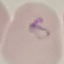
Summary:
  - Result: malaria parasites detected
  - Preparation: thin smear
  - Image type: automatically extracted cell patch, resized to 64 × 64 pixels
  - Stain: Giemsa
  - Capture: smartphone through the microscope eyepiece